Assess this cell for malaria.
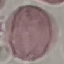
Uninfected.

Summary:
  - Stain: Giemsa
  - Capture: smartphone camera at the microscope eyepiece
  - Preparation: thin blood smear
  - Image type: cell patch, automatically extracted from a larger field of view and resized to 64 × 64 pixels